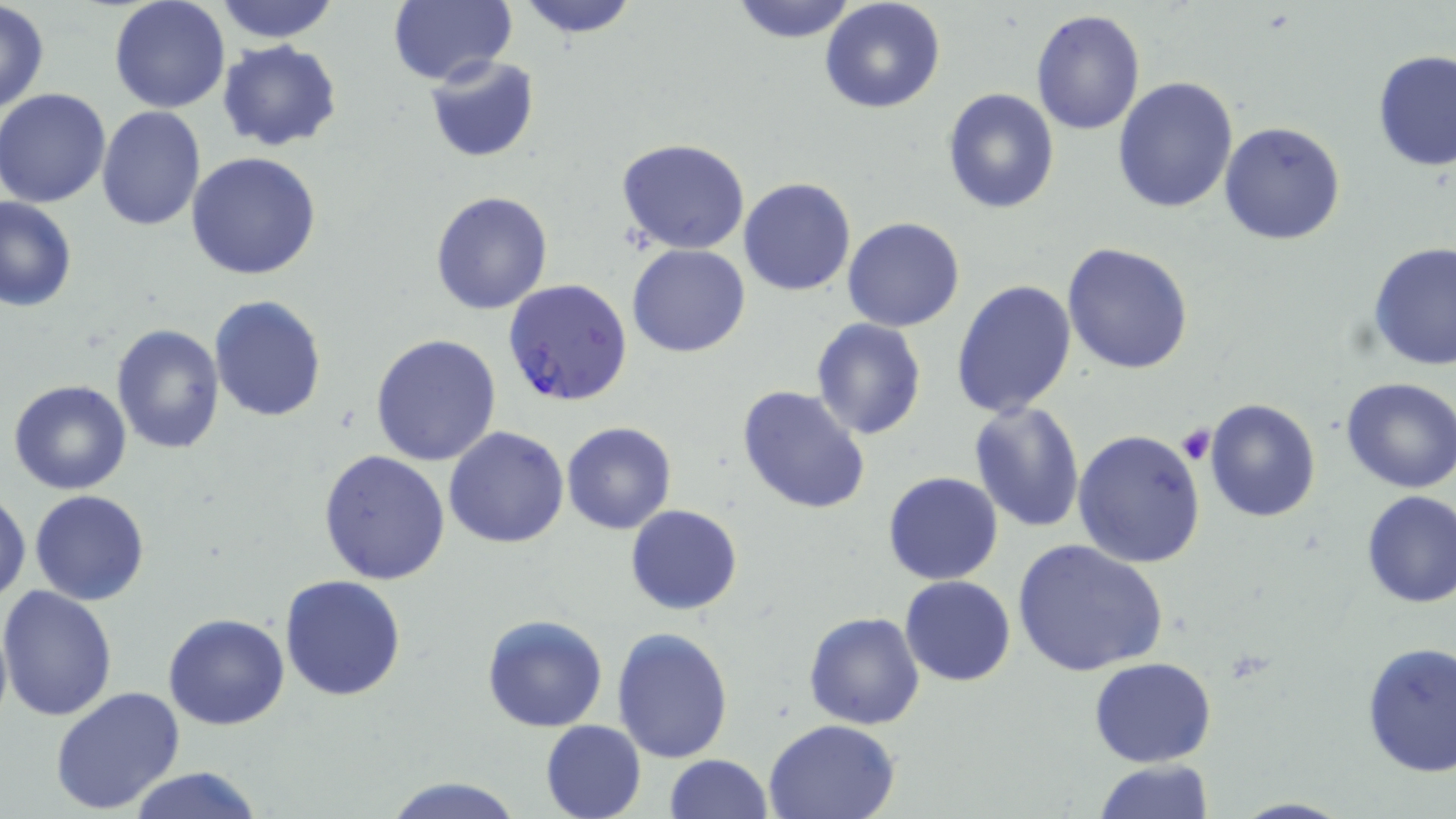

Summary:
  - Coordinate format: approximate bounding boxes as [x1, y1, x2, y2] in pixels
  - Uninfected red blood cell locations: [107, 0, 232, 113], [211, 0, 341, 43], [512, 0, 642, 37], [728, 0, 859, 43], [818, 0, 946, 114], [0, 2, 49, 115], [386, 2, 515, 87], [1030, 8, 1145, 137], [216, 40, 343, 152], [1372, 49, 1455, 171], [424, 54, 541, 163], [1112, 76, 1238, 215], [1, 88, 113, 207], [941, 89, 1060, 213], [97, 106, 204, 230], [1219, 121, 1346, 245], [614, 138, 752, 255], [186, 153, 324, 282], [738, 176, 855, 297], [430, 190, 555, 316], [0, 197, 77, 312], [843, 218, 965, 332], [1062, 241, 1195, 375], [1367, 243, 1455, 370], [626, 244, 750, 358], [950, 279, 1077, 420], [208, 296, 328, 423], [810, 319, 926, 439], [111, 323, 225, 453], [370, 334, 502, 468], [1339, 377, 1456, 494], [7, 381, 132, 496], [736, 384, 872, 516], [1204, 398, 1321, 522], [967, 402, 1087, 534], [561, 422, 677, 535], [443, 426, 570, 548], [1073, 428, 1205, 568], [317, 450, 451, 585], [882, 472, 1003, 586], [0, 488, 30, 605], [29, 490, 152, 606], [1360, 490, 1456, 607], [626, 505, 743, 615], [1012, 540, 1169, 677], [279, 574, 408, 701], [900, 576, 1016, 687], [1, 585, 120, 723], [804, 611, 927, 730], [163, 612, 291, 731], [481, 613, 609, 733], [611, 626, 736, 762], [1359, 643, 1455, 777], [1089, 657, 1217, 767], [50, 686, 187, 813], [763, 718, 901, 818], [540, 720, 648, 819], [663, 755, 773, 818], [1094, 759, 1214, 818], [124, 767, 263, 819], [382, 775, 527, 818], [1224, 797, 1355, 818]
  - Plasmodium falciparum-infected red blood cell locations: [504, 280, 633, 408]
  - Platelet locations: [1176, 423, 1216, 465]
  - Slide-level diagnosis: Plasmodium falciparum
  - Stain: May-Grünwald-Giemsa
  - Modality: optical microscopy
  - Field of view: one of a larger specimen
  - Magnification: 1000x
  - Image size: 1456×819 pixels
  - Preparation: thin blood smear